Classify this cell by malaria status.
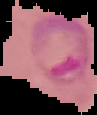

Parasitized.

Summary:
  - Image type: segmented cell region on a black background
  - Image size: 97×115 pixels
  - Preparation: thin blood film